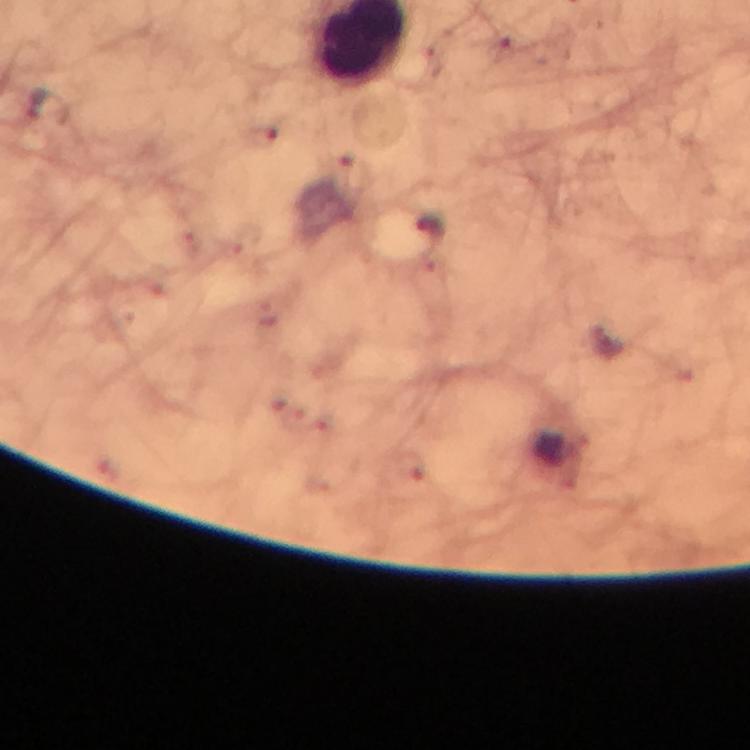 Approximate centers as (x, y) in pixels. Plasmodium parasite locations: (36, 103), (431, 228). Thick blood film. Photographed through the microscope with a smartphone camera. At 100x magnification. Immersion oil was used. Image is 750×750 pixels. From a malaria diagnostic workup. Giemsa-stained preparation. Cropped region of a single field of view.